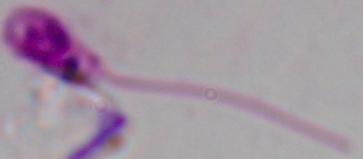

Summary:
  - Identification: Leishmania
  - Magnification: 1000x
  - Modality: micrograph